Classify this cell by malaria status.
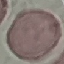
It is uninfected.

Thin blood smear. Automatically extracted cell patch, resized to 64 × 64 pixels. Photographed with a smartphone camera at the microscope eyepiece. Giemsa stain.